Outline each blood parasite and name the species.
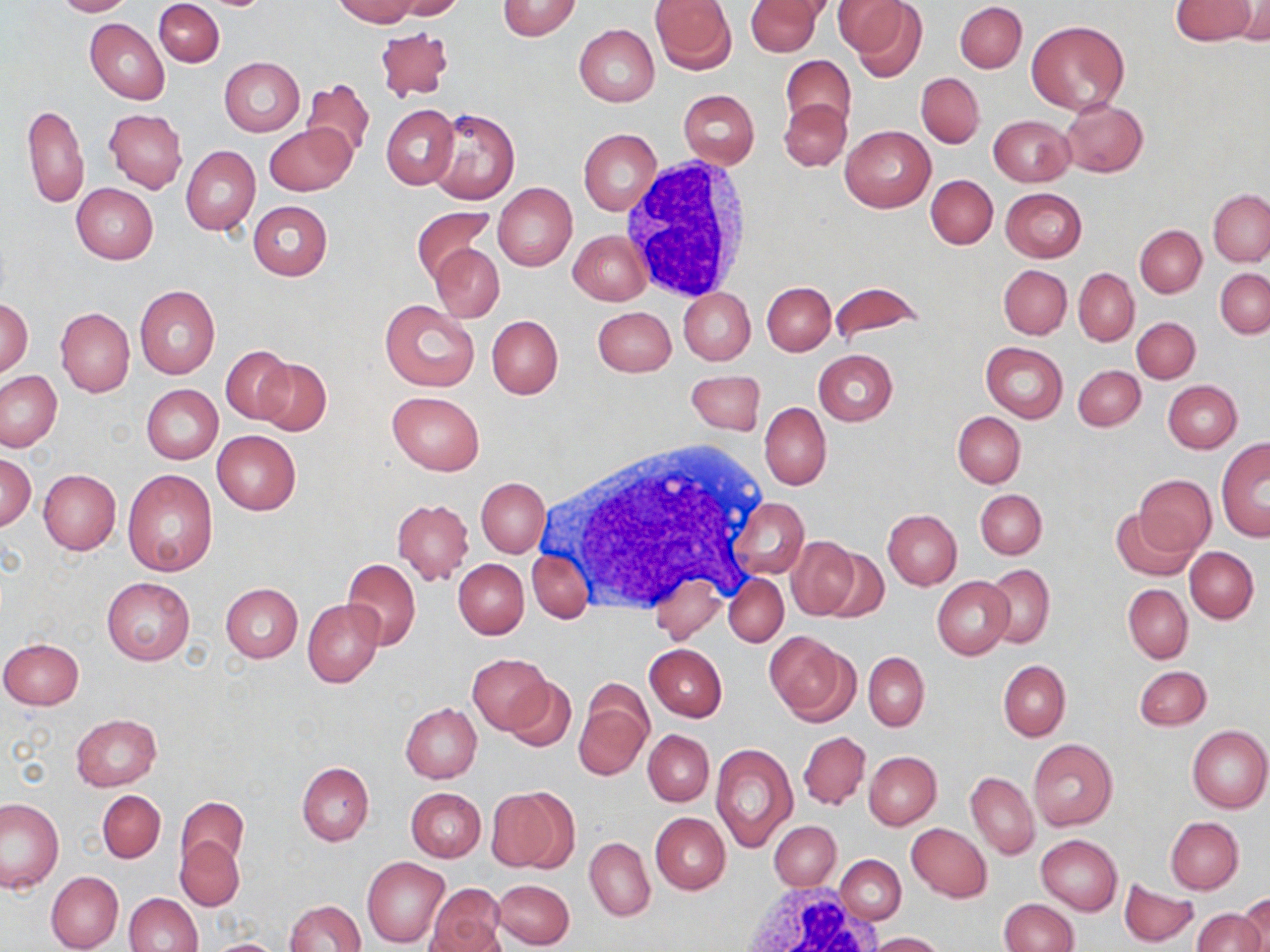

No blood parasites seen.

Summary:
  - Coordinate format: approximate bounding boxes as (x1, y1, x2, y2) in pixels
  - White blood cell locations: (618, 162, 754, 299), (545, 438, 770, 616), (742, 882, 882, 952)
  - Uninfected red blood cell locations: (52, 0, 132, 16), (154, 0, 223, 66), (332, 0, 418, 26), (392, 0, 465, 19), (649, 0, 737, 74), (745, 0, 821, 56), (838, 0, 925, 76), (1170, 0, 1257, 45), (497, 1, 582, 39), (955, 2, 1026, 72), (1232, 2, 1269, 43), (952, 6, 1097, 84), (85, 18, 169, 104), (1026, 19, 1129, 115), (375, 24, 453, 104), (574, 24, 659, 106), (780, 55, 856, 133), (220, 58, 305, 136), (916, 73, 984, 147), (300, 78, 374, 165), (678, 89, 758, 168), (779, 99, 851, 171), (1060, 99, 1148, 177), (21, 102, 88, 209), (382, 105, 458, 189), (426, 108, 520, 204), (106, 109, 187, 193), (989, 114, 1076, 186), (264, 123, 356, 196), (840, 125, 934, 213), (578, 129, 662, 215), (181, 146, 260, 236), (926, 175, 998, 248), (493, 182, 577, 271), (71, 183, 157, 265), (1001, 189, 1087, 263), (1208, 189, 1270, 266), (248, 200, 332, 281), (411, 206, 493, 283), (1135, 225, 1206, 297), (569, 230, 651, 305), (431, 242, 504, 323), (999, 264, 1072, 339), (1215, 268, 1270, 339), (1074, 269, 1139, 344), (762, 281, 835, 354), (830, 282, 924, 344), (135, 286, 220, 379), (679, 288, 755, 364), (1, 297, 33, 377), (380, 298, 479, 391), (56, 307, 134, 398), (592, 307, 676, 377), (486, 315, 563, 399), (1132, 316, 1200, 382), (980, 342, 1068, 422), (221, 346, 293, 423), (814, 349, 897, 426), (255, 359, 331, 436), (1074, 365, 1145, 430), (686, 370, 766, 436), (1, 371, 63, 451), (1164, 381, 1242, 452), (142, 385, 223, 464), (387, 391, 485, 475), (759, 402, 831, 490), (953, 412, 1025, 488), (212, 430, 301, 515), (1216, 436, 1270, 541), (0, 453, 36, 530), (38, 469, 120, 554), (122, 470, 217, 575), (1133, 474, 1216, 555), (477, 478, 549, 557), (976, 489, 1046, 559), (731, 497, 809, 579), (392, 498, 473, 584), (1110, 506, 1197, 581), (883, 510, 962, 589), (787, 537, 861, 619), (1185, 546, 1258, 623), (819, 548, 889, 622), (527, 549, 593, 623), (342, 558, 421, 651), (453, 559, 528, 638), (984, 563, 1054, 648), (724, 572, 788, 646), (649, 576, 725, 642), (932, 576, 1014, 659), (100, 578, 194, 665), (221, 582, 302, 663), (1123, 584, 1193, 663), (303, 598, 383, 687), (764, 630, 855, 723), (0, 637, 85, 709), (646, 643, 727, 721), (863, 652, 929, 730), (467, 654, 553, 733), (998, 661, 1070, 739), (1135, 665, 1211, 730), (505, 678, 576, 753), (575, 681, 653, 782), (400, 702, 481, 783), (70, 714, 162, 792), (1186, 725, 1270, 813), (643, 729, 713, 805), (799, 731, 871, 810), (1028, 738, 1118, 830), (710, 742, 797, 852), (864, 751, 940, 829), (297, 762, 374, 846), (966, 771, 1040, 860), (489, 787, 575, 874), (407, 788, 485, 861), (98, 790, 165, 863), (176, 796, 246, 870), (1, 797, 65, 893), (650, 812, 730, 894), (1165, 816, 1243, 893), (769, 822, 840, 891), (907, 823, 992, 902), (586, 832, 724, 915), (1036, 835, 1122, 914), (175, 837, 244, 911), (585, 838, 655, 921), (362, 856, 450, 948), (835, 856, 906, 924), (45, 871, 123, 952), (493, 879, 574, 948), (1119, 880, 1199, 947), (428, 886, 505, 950), (123, 893, 202, 952), (1238, 895, 1270, 951), (284, 899, 364, 951), (998, 899, 1078, 952), (1193, 907, 1265, 952), (426, 920, 504, 952), (870, 932, 944, 951), (204, 938, 287, 952)
  - Slide-level diagnosis: no evidence of blood parasites
  - Modality: optical microscopy
  - Field of view: single
  - Preparation: thin blood film
  - Stain: May-Grünwald-Giemsa
  - Magnification: 1000x
  - Image size: 1270×952 pixels